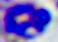

Summary:
  - Modality: photomicrograph
  - Magnification: 400x
  - Identification: white blood cell